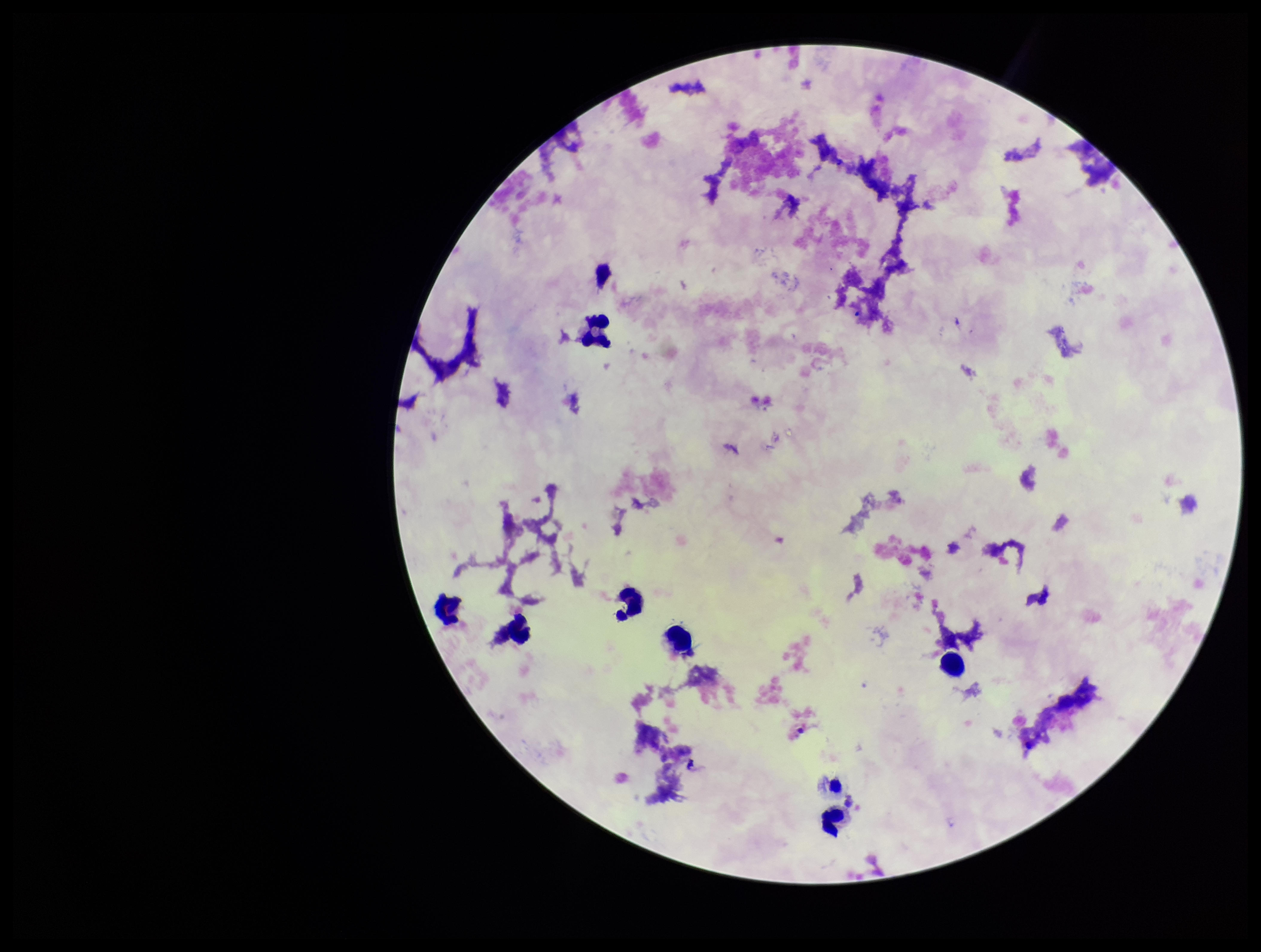

Photographed through the microscope eyepiece with a smartphone camera. Plasmodium parasites: none identified. Stained with Giemsa. Image is 1261×952 pixels. Leukocyte count: 7. Preparation: thick. One field from this slide. Patient malaria status: negative. Parasite count: 0.